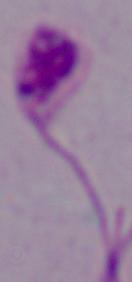
Summary:
  - Identification: Leishmania
  - Modality: micrograph
  - Magnification: 1000x